Mark where leukocytes are.
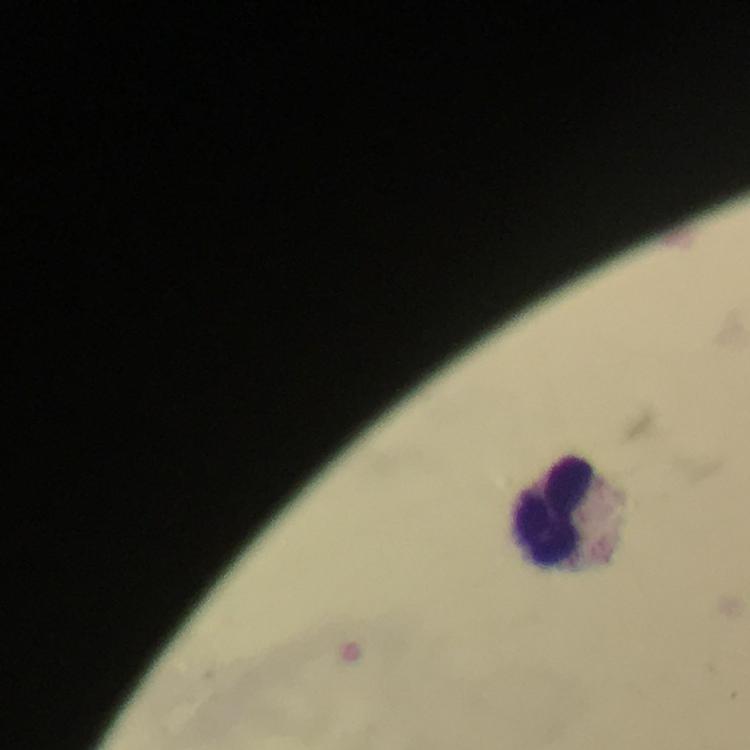
Approximate centers as (x, y) in pixels.
Leukocytes: (552, 511).

Summary:
  - Capture: smartphone mounted on the microscope
  - Preparation: thick smear
  - Image size: 750×750 pixels
  - Magnification: 100x
  - Context: from a diagnostic examination for malaria
  - Immersion oil: applied
  - Stain: Giemsa
  - Plasmodium parasites: none detected
  - Cropped from: a single field of view